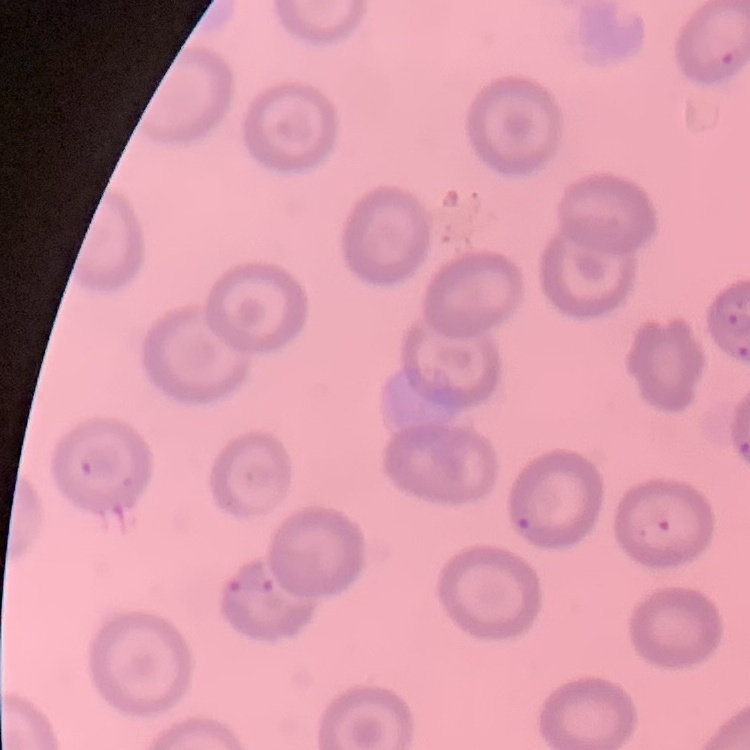 The red blood cells show no rouleaux formation. Thin blood smear. Stained with either Field's or Giemsa. Square crop of a larger photomicrograph.